State which parasite is depicted.
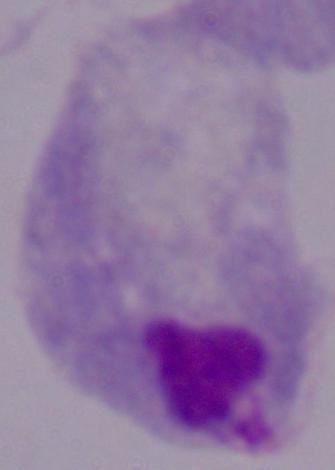
A trichomonad.

Summary:
  - Magnification: 1000x
  - Modality: photomicrograph